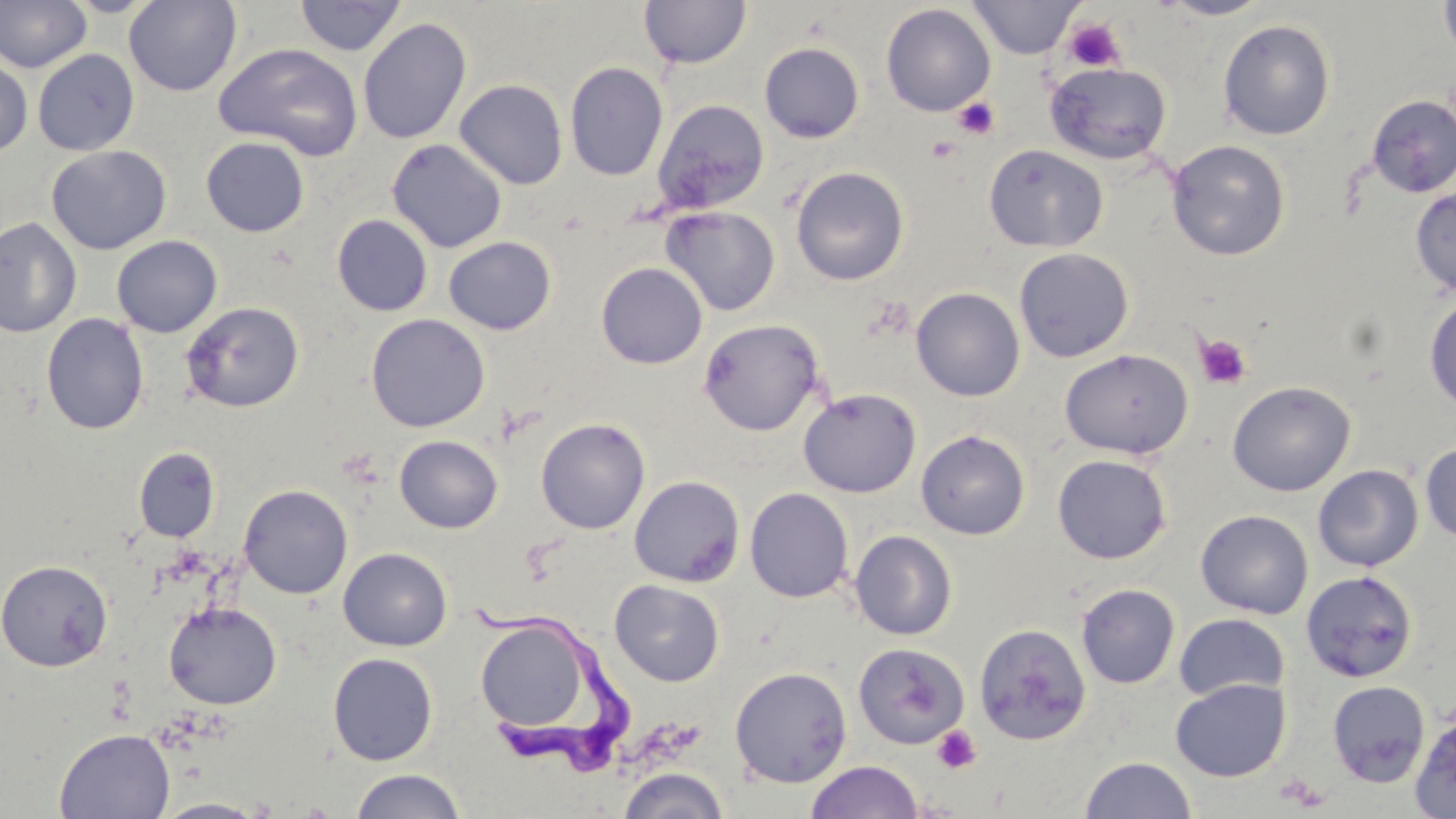
Approximate bounding boxes as (x1,y1)-(x2,y2) corner pairs in pixels. Trypanosoma brucei locations: (467,600)-(637,785). Platelet locations: (1063,18)-(1125,72), (953,97)-(1000,139), (926,136)-(961,164), (1194,334)-(1253,390), (931,725)-(981,774). Uninfected red blood cell locations: (0,0)-(92,73), (62,0)-(162,17), (124,0)-(242,96), (294,0)-(407,56), (639,0)-(752,69), (1157,0)-(1274,20), (1438,0)-(1456,62), (968,1)-(1083,59), (881,3)-(995,117), (358,17)-(471,145), (1217,18)-(1336,140), (759,42)-(865,143), (213,43)-(364,161), (33,49)-(140,156), (0,56)-(33,156), (565,61)-(668,181), (1044,61)-(1172,165), (454,79)-(569,189), (1366,94)-(1456,197), (652,99)-(769,215), (200,136)-(309,237), (386,138)-(508,253), (1166,139)-(1291,261), (983,144)-(1109,253), (46,145)-(171,255), (790,166)-(909,286), (1410,187)-(1456,296), (661,206)-(780,316), (332,214)-(433,316), (0,216)-(82,338), (111,235)-(223,338), (444,237)-(556,335), (1013,247)-(1135,363), (595,262)-(708,369), (911,287)-(1025,401), (1424,294)-(1456,413), (180,301)-(304,413), (41,313)-(149,434), (366,314)-(489,432), (697,318)-(826,436), (1059,348)-(1194,460), (1226,381)-(1356,497), (798,387)-(921,498), (535,417)-(650,534), (916,429)-(1030,540), (394,435)-(503,533), (1419,442)-(1456,544), (134,447)-(220,542), (1052,454)-(1172,564), (1313,464)-(1423,572), (629,475)-(745,587), (239,484)-(353,598), (744,487)-(854,603), (1195,509)-(1313,619), (849,530)-(957,640), (338,547)-(452,651), (0,558)-(114,672), (1300,569)-(1418,683), (609,580)-(724,687), (1076,583)-(1180,689), (163,602)-(282,709), (1174,613)-(1289,702), (475,616)-(596,736), (973,623)-(1091,745), (852,641)-(969,749), (327,652)-(438,765), (729,666)-(852,788), (1170,679)-(1291,782), (1327,680)-(1431,787), (1411,712)-(1456,818), (54,728)-(176,819), (1079,755)-(1197,818), (806,759)-(924,819), (617,766)-(731,819), (348,769)-(468,819), (150,797)-(273,818). Slide-level diagnosis: Trypanosoma brucei. Image is 1456×819 pixels. May-Grünwald-Giemsa stain. One field of a larger specimen. Optical microscopy. Captured at 1000x magnification. Thin blood smear.